Give the extent of all Plasmodium ovale-infected red blood cells.
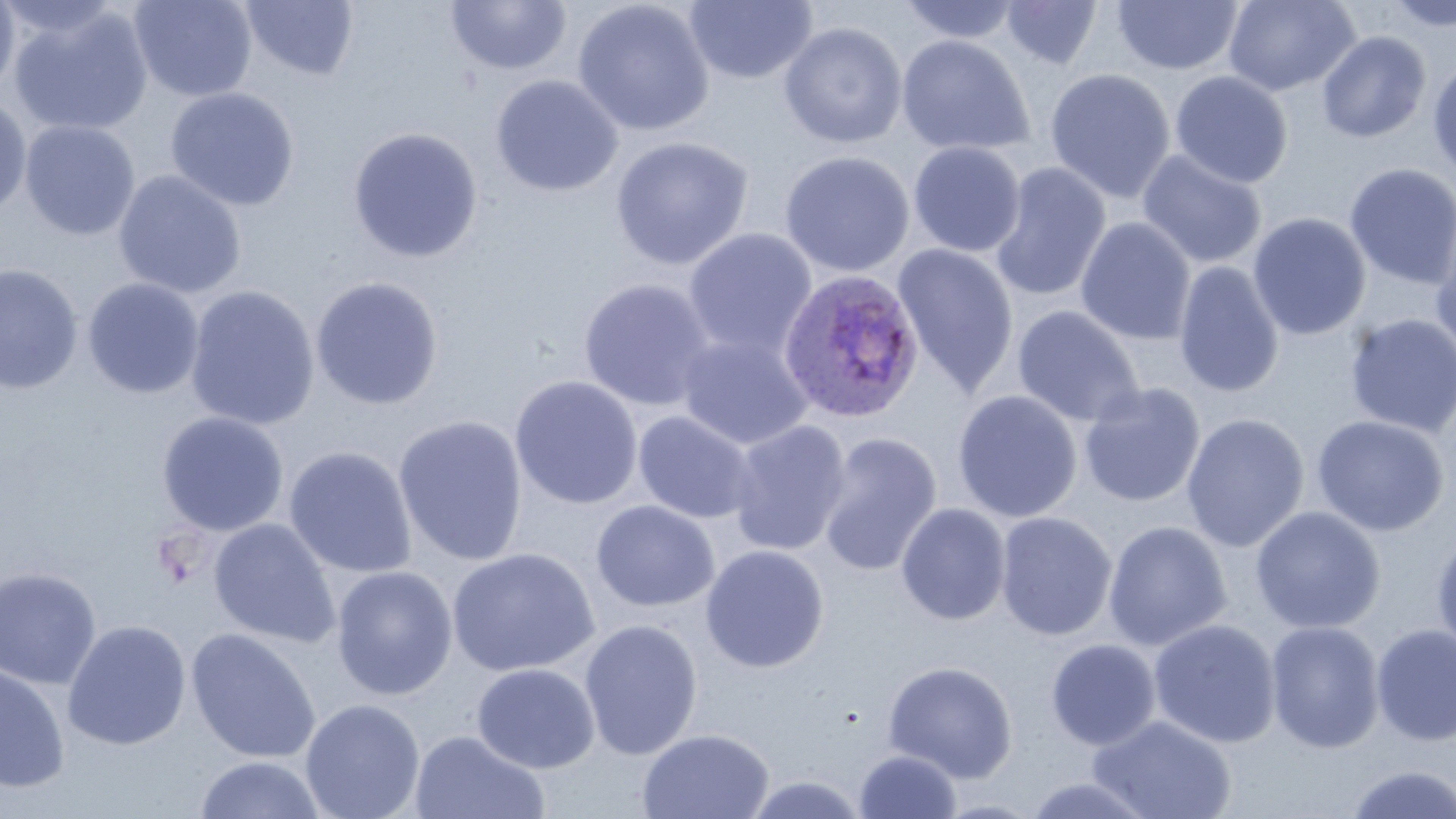

Approximate bounding boxes as (x1, y1, x2, y2) in pixels.
Plasmodium ovale-infected red blood cells: (777, 268, 926, 423).

slide_level_diagnosis: Plasmodium ovale
preparation: thin blood film
uninfected_red_blood_cell_locations: 'approximate bounding boxes as (x1, y1, x2, y2) in pixels: (129, 0, 257, 102), (896, 0, 1024, 44), (1223, 0, 1359, 96), (1382, 0, 1456, 32), (0, 1, 20, 102), (239, 1, 360, 81), (445, 1, 572, 76), (572, 1, 715, 137), (684, 1, 817, 85), (999, 1, 1103, 70), (1112, 1, 1243, 75), (142, 4, 269, 191), (8, 5, 154, 137), (778, 21, 908, 149), (1316, 31, 1431, 143), (896, 35, 1034, 156), (1427, 58, 1456, 181), (1044, 68, 1176, 204), (1169, 71, 1293, 188), (491, 75, 623, 197), (165, 87, 300, 212), (0, 94, 32, 218), (19, 120, 141, 241), (347, 127, 484, 263), (610, 136, 754, 270), (908, 141, 1026, 257), (1137, 149, 1267, 270), (779, 150, 915, 277), (989, 162, 1111, 303), (1343, 162, 1456, 289), (113, 170, 247, 299), (1248, 212, 1371, 340), (1076, 217, 1196, 346), (1431, 226, 1456, 364), (682, 228, 818, 360), (892, 244, 1019, 397), (1173, 261, 1285, 398), (0, 263, 83, 395), (310, 276, 444, 410), (82, 277, 205, 399), (578, 278, 718, 412), (183, 285, 320, 431), (1011, 305, 1145, 427), (1344, 313, 1456, 437), (676, 333, 815, 452), (509, 375, 644, 510), (1078, 382, 1206, 508), (952, 389, 1083, 523), (633, 410, 757, 524), (156, 411, 290, 536), (1181, 413, 1309, 552), (393, 414, 528, 566), (1311, 415, 1449, 536), (727, 420, 851, 556), (817, 431, 943, 577), (283, 446, 417, 579), (591, 500, 720, 613), (896, 503, 1011, 625), (1250, 506, 1386, 634), (995, 511, 1118, 641), (208, 518, 341, 648), (1102, 520, 1232, 651), (1430, 531, 1456, 659), (699, 544, 830, 673), (446, 548, 600, 677), (331, 566, 458, 700), (0, 567, 102, 689), (1148, 618, 1282, 749), (62, 619, 192, 750), (578, 619, 703, 760), (1265, 621, 1385, 753), (1370, 624, 1456, 747), (185, 627, 322, 763), (1045, 639, 1161, 750), (881, 660, 1019, 782), (0, 662, 70, 793), (472, 662, 600, 773), (300, 698, 425, 819), (1088, 714, 1237, 818), (637, 727, 774, 819), (409, 730, 551, 819), (853, 749, 963, 818), (193, 755, 328, 819), (1342, 764, 1456, 818), (739, 773, 871, 818), (1020, 775, 1160, 819)'
stain: May-Grünwald-Giemsa
modality: light microscopy
field_of_view: one of a larger specimen
image_size: 1456×819 pixels
magnification: 1000x